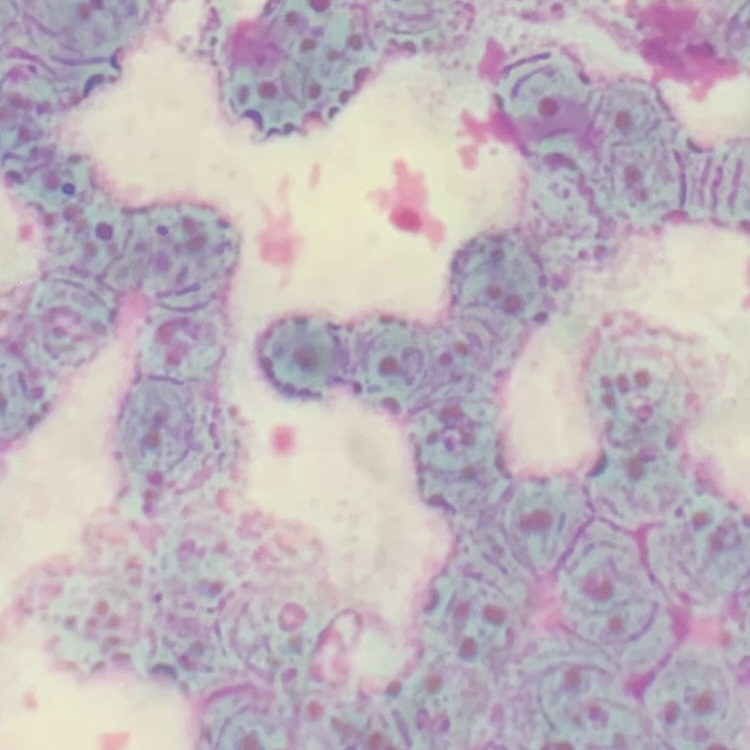 The red blood cells show rouleaux formation. Square crop of a larger photomicrograph. Field's or Giemsa stain. Thin blood smear.